Locate every blood parasite and identify its species.
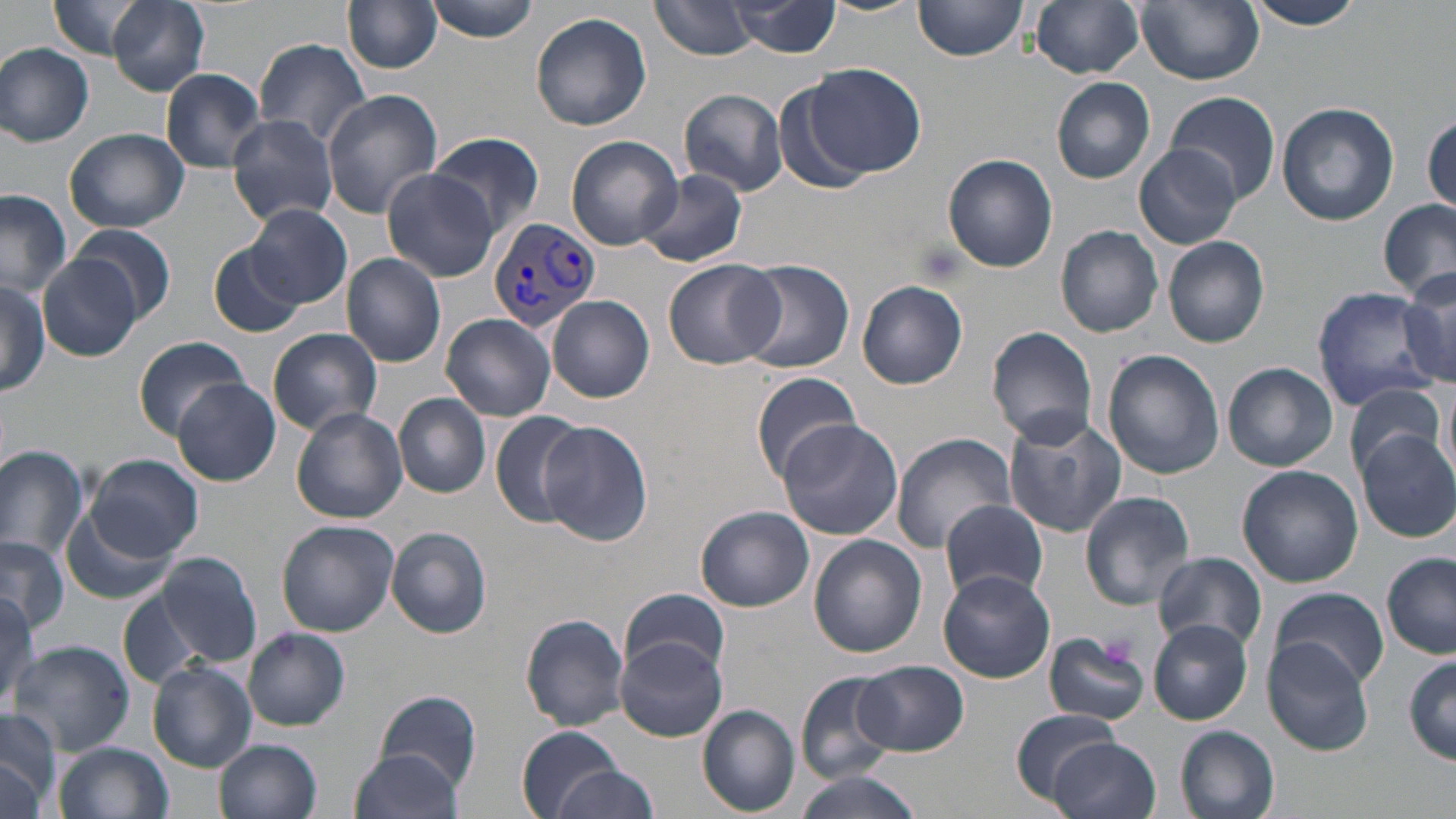

Approximate bounding boxes as named x1/y1/x2/y2 corners in pixels.
Plasmodium vivax-infected red blood cells: (x1=487, y1=218, x2=600, y2=331).
No Plasmodium falciparum, Plasmodium ovale, Plasmodium malariae, Babesia divergens, or Trypanosoma brucei observed.

Platelet locations: (x1=1097, y1=632, x2=1138, y2=669). Uninfected red blood cell locations: (x1=46, y1=0, x2=153, y2=60), (x1=107, y1=0, x2=210, y2=93), (x1=425, y1=0, x2=542, y2=42), (x1=648, y1=0, x2=759, y2=59), (x1=726, y1=0, x2=841, y2=58), (x1=817, y1=0, x2=922, y2=17), (x1=914, y1=0, x2=1029, y2=61), (x1=1136, y1=0, x2=1265, y2=85), (x1=1247, y1=0, x2=1368, y2=28), (x1=342, y1=1, x2=443, y2=74), (x1=1029, y1=1, x2=1146, y2=78), (x1=531, y1=11, x2=652, y2=131), (x1=253, y1=39, x2=372, y2=151), (x1=0, y1=43, x2=94, y2=146), (x1=805, y1=64, x2=927, y2=178), (x1=161, y1=68, x2=268, y2=172), (x1=1053, y1=76, x2=1156, y2=184), (x1=678, y1=88, x2=789, y2=198), (x1=321, y1=90, x2=443, y2=217), (x1=1165, y1=90, x2=1280, y2=205), (x1=1277, y1=101, x2=1397, y2=225), (x1=1424, y1=113, x2=1456, y2=213), (x1=226, y1=114, x2=339, y2=226), (x1=66, y1=128, x2=188, y2=233), (x1=429, y1=131, x2=543, y2=238), (x1=564, y1=136, x2=685, y2=252), (x1=1135, y1=145, x2=1244, y2=249), (x1=942, y1=153, x2=1058, y2=274), (x1=637, y1=168, x2=748, y2=269), (x1=381, y1=170, x2=501, y2=281), (x1=0, y1=190, x2=73, y2=297), (x1=1379, y1=198, x2=1456, y2=303), (x1=246, y1=203, x2=351, y2=307), (x1=68, y1=223, x2=177, y2=324), (x1=1057, y1=225, x2=1163, y2=337), (x1=1162, y1=235, x2=1271, y2=348), (x1=207, y1=244, x2=307, y2=339), (x1=40, y1=253, x2=145, y2=360), (x1=342, y1=254, x2=447, y2=366), (x1=662, y1=258, x2=782, y2=369), (x1=729, y1=259, x2=856, y2=375), (x1=1397, y1=269, x2=1456, y2=389), (x1=0, y1=278, x2=52, y2=395), (x1=856, y1=281, x2=968, y2=390), (x1=1311, y1=289, x2=1439, y2=410), (x1=548, y1=294, x2=655, y2=403), (x1=441, y1=315, x2=555, y2=421), (x1=987, y1=326, x2=1099, y2=447), (x1=268, y1=327, x2=383, y2=435), (x1=134, y1=335, x2=251, y2=440), (x1=1102, y1=349, x2=1224, y2=480), (x1=1222, y1=362, x2=1338, y2=472), (x1=750, y1=370, x2=863, y2=483), (x1=1439, y1=378, x2=1455, y2=482), (x1=171, y1=379, x2=281, y2=486), (x1=1343, y1=380, x2=1446, y2=480), (x1=394, y1=393, x2=491, y2=497), (x1=292, y1=408, x2=407, y2=523), (x1=488, y1=410, x2=590, y2=529), (x1=1001, y1=412, x2=1129, y2=538), (x1=538, y1=420, x2=654, y2=547), (x1=777, y1=421, x2=903, y2=540), (x1=1357, y1=430, x2=1456, y2=542), (x1=890, y1=433, x2=1017, y2=553), (x1=0, y1=444, x2=89, y2=561), (x1=87, y1=453, x2=204, y2=561), (x1=1237, y1=465, x2=1363, y2=588), (x1=1079, y1=490, x2=1196, y2=608), (x1=937, y1=499, x2=1049, y2=603), (x1=695, y1=505, x2=814, y2=612), (x1=60, y1=506, x2=179, y2=606), (x1=277, y1=519, x2=399, y2=637), (x1=386, y1=526, x2=493, y2=639), (x1=0, y1=535, x2=70, y2=634), (x1=808, y1=535, x2=926, y2=658), (x1=153, y1=551, x2=263, y2=670), (x1=1152, y1=552, x2=1268, y2=652), (x1=1382, y1=553, x2=1456, y2=658), (x1=939, y1=570, x2=1056, y2=683), (x1=1269, y1=586, x2=1388, y2=690), (x1=117, y1=588, x2=209, y2=688), (x1=620, y1=590, x2=731, y2=678), (x1=0, y1=591, x2=41, y2=713), (x1=520, y1=613, x2=630, y2=731), (x1=1147, y1=618, x2=1253, y2=725), (x1=243, y1=627, x2=350, y2=730), (x1=1044, y1=632, x2=1152, y2=726), (x1=616, y1=635, x2=727, y2=742), (x1=1261, y1=640, x2=1374, y2=756), (x1=9, y1=641, x2=134, y2=756), (x1=1404, y1=655, x2=1456, y2=765), (x1=150, y1=661, x2=256, y2=772), (x1=854, y1=661, x2=968, y2=756), (x1=797, y1=670, x2=901, y2=785), (x1=376, y1=690, x2=481, y2=793), (x1=698, y1=705, x2=801, y2=815), (x1=0, y1=709, x2=63, y2=814), (x1=1011, y1=709, x2=1121, y2=806), (x1=517, y1=726, x2=627, y2=818), (x1=1176, y1=726, x2=1281, y2=819), (x1=1047, y1=737, x2=1161, y2=819), (x1=214, y1=739, x2=323, y2=819), (x1=54, y1=741, x2=173, y2=819), (x1=349, y1=746, x2=466, y2=819), (x1=0, y1=756, x2=45, y2=817), (x1=555, y1=766, x2=659, y2=818), (x1=791, y1=770, x2=929, y2=819). Slide-level diagnosis: Plasmodium vivax. Thin blood film. 1000x magnification. Optical microscopy. May-Grünwald-Giemsa-stained preparation. Single field of view. Image is 1456×819 pixels.